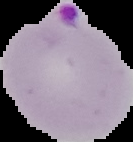
Summary:
  - Result: malaria parasites identified
  - Preparation: thin blood film
  - Image size: 133×142 pixels
  - Image type: segmented cell region on a black background